Identify the cell.
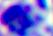
A leukocyte.

{
  "modality": "photomicrograph",
  "magnification": "400x"
}